Locate every blood parasite and identify its species.
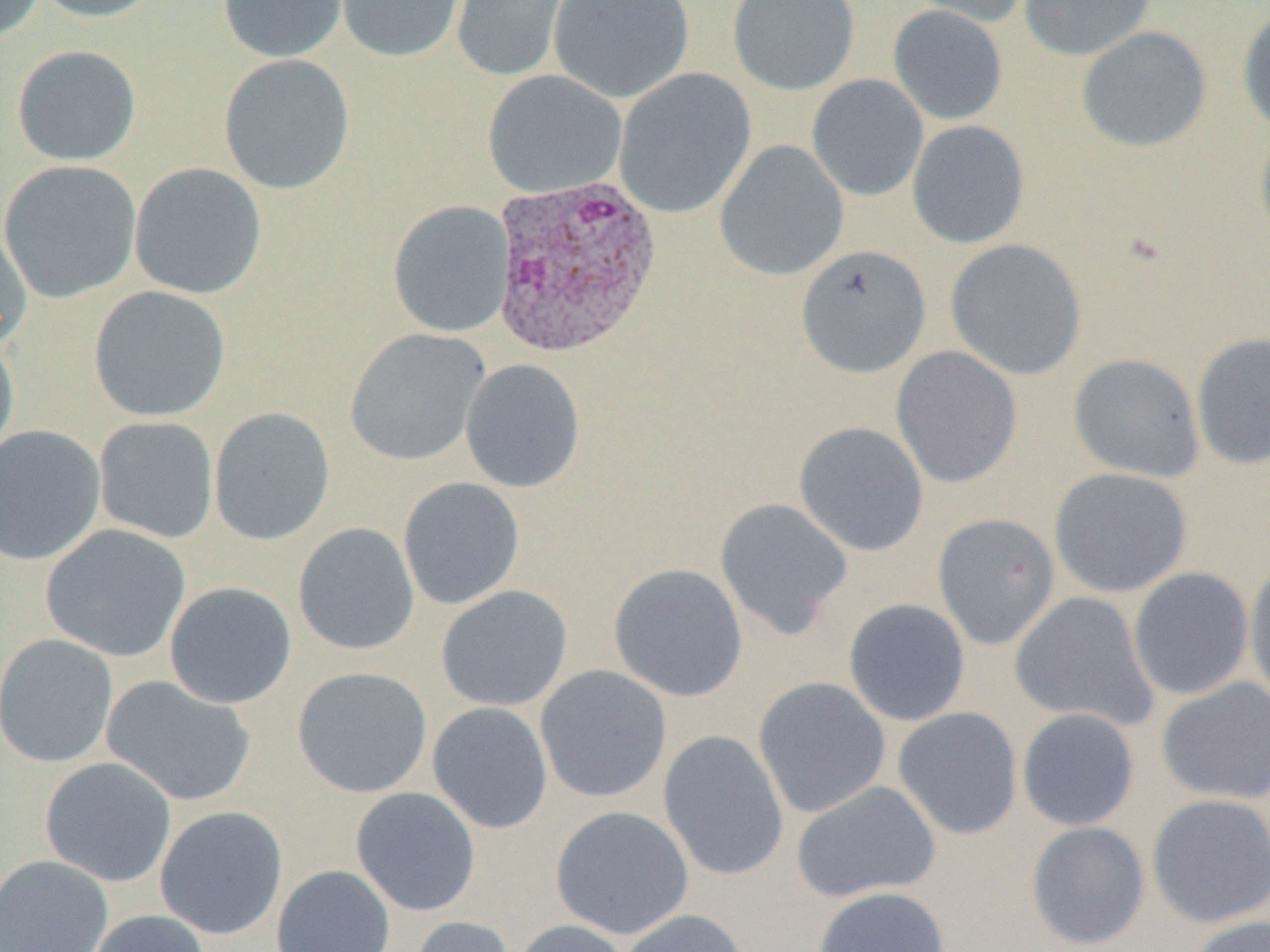

Approximate bounding boxes as (x1, y1, x2, y2) in pixels.
Plasmodium ovale-infected red blood cells: (489, 174, 663, 358).
No Plasmodium falciparum, Plasmodium malariae, Plasmodium vivax, Babesia divergens, or Trypanosoma brucei observed.

{
  "slide_level_diagnosis": "Plasmodium ovale",
  "magnification": "1000x",
  "field_of_view": "one of a larger specimen",
  "uninfected_red_blood_cell_locations": "approximate bounding boxes as (x1, y1, x2, y2) in pixels: (0, 0, 45, 45), (28, 0, 168, 23), (218, 0, 348, 62), (334, 0, 466, 63), (450, 0, 574, 83), (549, 0, 695, 103), (727, 0, 860, 95), (903, 0, 1033, 29), (1018, 0, 1156, 61), (887, 5, 1008, 125), (1237, 8, 1270, 135), (1076, 25, 1212, 153), (11, 45, 142, 166), (218, 54, 356, 195), (613, 68, 757, 219), (482, 70, 627, 198), (806, 74, 929, 202), (907, 120, 1030, 249), (1255, 122, 1270, 245), (715, 140, 849, 281), (1, 160, 142, 304), (129, 163, 268, 300), (388, 200, 515, 338), (0, 219, 33, 353), (945, 239, 1086, 380), (795, 245, 932, 378), (88, 286, 231, 422), (344, 328, 490, 467), (0, 332, 19, 464), (1191, 332, 1270, 470), (890, 346, 1022, 488), (1068, 353, 1205, 482), (460, 359, 586, 493), (209, 407, 336, 546), (93, 416, 219, 544), (794, 422, 928, 556), (0, 425, 106, 566), (1048, 467, 1192, 598), (398, 477, 526, 610), (714, 498, 853, 639), (932, 513, 1060, 649), (292, 522, 420, 656), (40, 524, 191, 663), (1244, 558, 1270, 705), (608, 563, 748, 702), (1128, 567, 1254, 700), (164, 582, 297, 709), (436, 585, 573, 712), (1010, 592, 1160, 731), (843, 599, 970, 726), (0, 633, 119, 769), (535, 665, 672, 803), (292, 667, 433, 798), (101, 675, 257, 807), (753, 677, 892, 818), (1156, 677, 1270, 805), (427, 702, 554, 834), (892, 707, 1023, 839), (1016, 708, 1140, 831), (658, 730, 789, 881), (39, 757, 177, 887), (790, 780, 941, 903), (350, 787, 481, 917), (1146, 794, 1270, 928), (550, 805, 694, 939), (154, 806, 288, 940), (1026, 821, 1150, 950), (0, 855, 113, 952), (271, 864, 396, 952), (812, 886, 951, 952), (617, 909, 749, 952), (84, 910, 212, 952), (406, 915, 516, 952), (1186, 915, 1270, 952), (510, 920, 631, 952)",
  "preparation": "thin blood film",
  "image_size": "1270×952 pixels",
  "modality": "optical microscopy"
}